Describe the morphology of the red blood cells.
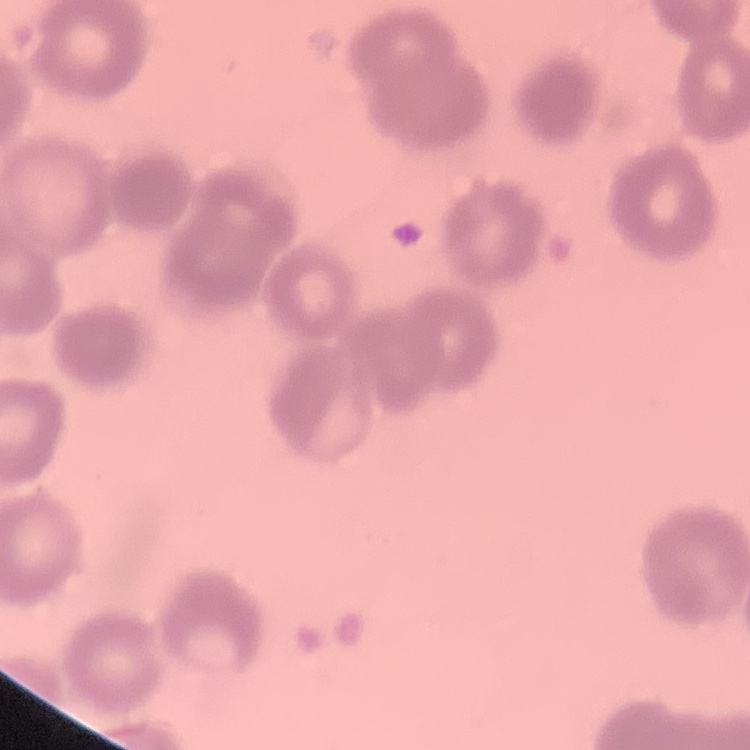
Rouleaux formation.

preparation = thin blood film
stain = Field's or Giemsa
image type = one tile cut from a larger photomicrograph